Name the parasite shown.
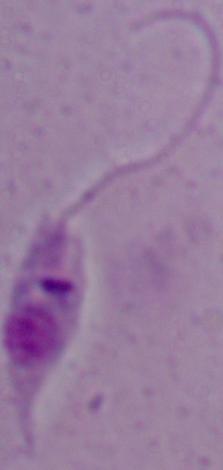

Leishmania.

Micrograph. 1000x magnification.